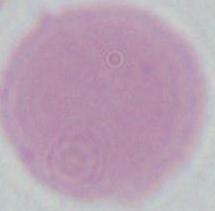
1000x magnification. An erythrocyte is shown. Micrograph.